Assess the morphology of the erythrocytes.
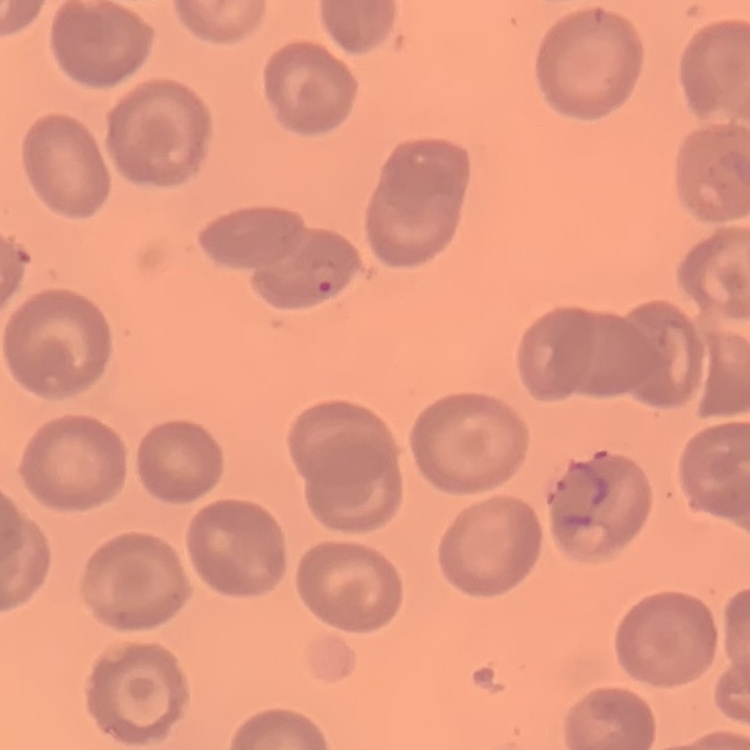

They show no rouleaux formation.

Field's or Giemsa stain. Square crop of a larger photomicrograph. Thin peripheral smear.